State which parasite is depicted.
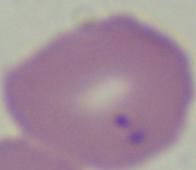

This is Babesia.

Summary:
  - Modality: micrograph
  - Magnification: 1000x